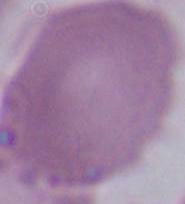
Summary:
  - Magnification: 1000x
  - Modality: micrograph
  - Identification: red blood cell